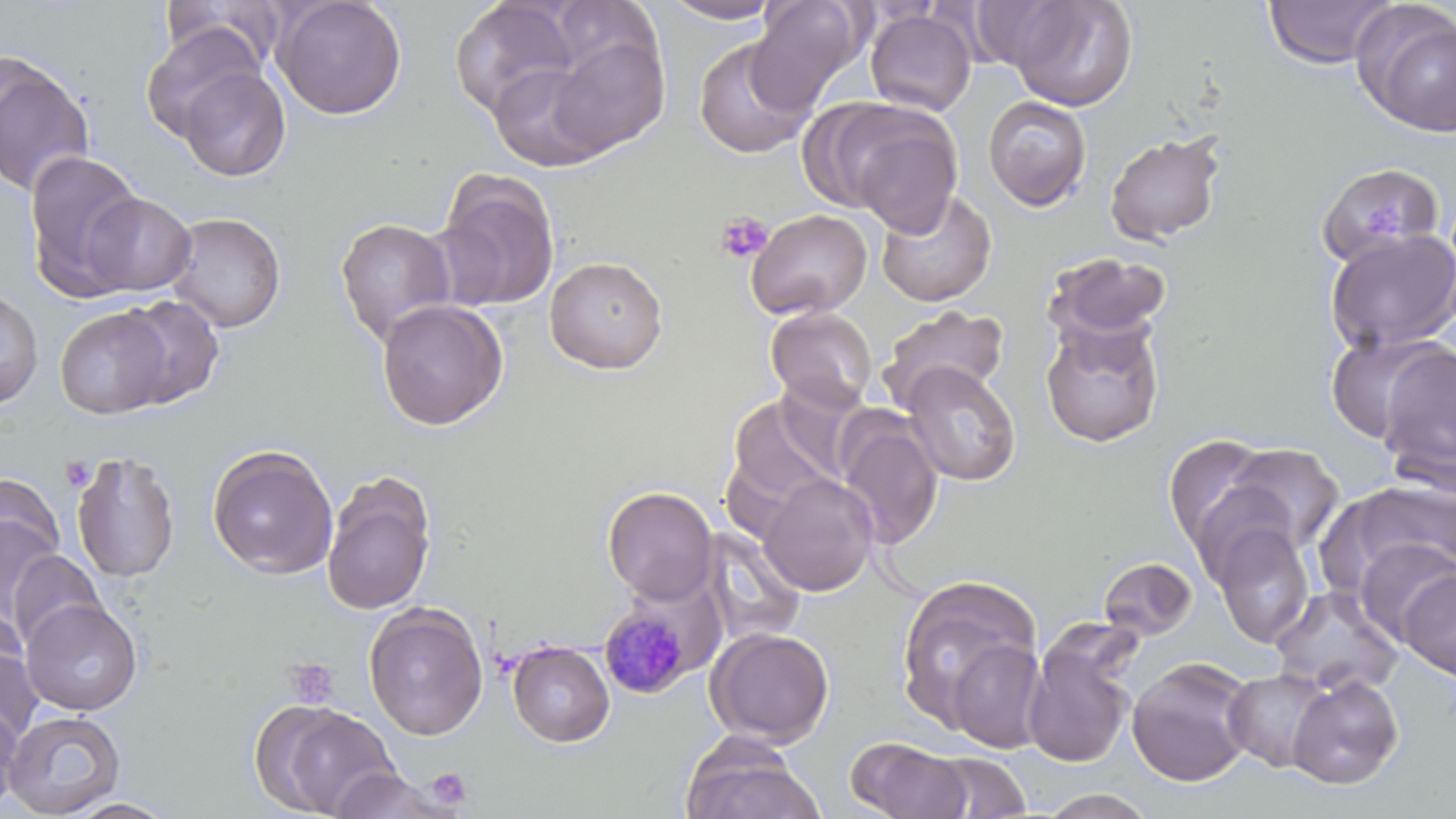

Summary:
  - Coordinate format: approximate bounding boxes as (x1,y1)-(x2,y2) corner pairs in pixels
  - Plasmodium malariae-infected red blood cell locations: (598,603)-(697,700)
  - Uninfected red blood cell locations: (273,0)-(407,120), (657,0)-(783,24), (746,0)-(867,110), (1005,0)-(1139,111), (1263,0)-(1398,69), (161,1)-(290,72), (448,1)-(579,119), (1352,3)-(1456,136), (865,9)-(977,116), (140,22)-(265,143), (541,31)-(671,155), (693,35)-(816,159), (0,51)-(95,198), (488,59)-(609,173), (178,66)-(292,182), (810,95)-(961,224), (982,95)-(1091,211), (1105,131)-(1226,245), (23,149)-(145,299), (1316,162)-(1445,269), (437,170)-(561,311), (875,189)-(997,307), (80,192)-(197,297), (746,208)-(873,320), (165,211)-(286,333), (335,216)-(457,347), (1325,227)-(1456,353), (1043,250)-(1172,344), (545,256)-(668,374), (0,289)-(43,409), (116,294)-(225,409), (376,299)-(508,430), (876,304)-(1011,412), (765,305)-(878,412), (54,306)-(173,419), (1041,317)-(1165,447), (1326,331)-(1451,445), (1377,344)-(1456,489), (901,361)-(1021,486), (726,395)-(845,510), (728,400)-(941,532), (835,411)-(943,550), (1163,434)-(1277,553), (1219,442)-(1346,560), (206,443)-(339,579), (70,449)-(181,583), (320,473)-(436,617), (758,473)-(878,596), (0,474)-(65,572), (1331,479)-(1456,586), (602,486)-(719,603), (0,510)-(64,626), (1210,523)-(1315,648), (699,526)-(807,648), (1354,537)-(1456,644), (5,550)-(106,652), (1098,556)-(1198,641), (1399,569)-(1456,681), (894,575)-(1044,731), (1270,586)-(1403,698), (21,598)-(143,716), (363,602)-(488,741), (0,606)-(29,704), (705,627)-(834,746), (1023,630)-(1139,769), (1,632)-(42,744), (946,639)-(1048,753), (507,640)-(615,747), (1126,656)-(1256,787), (1223,668)-(1334,773), (1286,674)-(1404,790), (255,699)-(400,818), (0,701)-(22,815), (3,709)-(126,817), (847,737)-(972,819), (680,740)-(826,819), (922,752)-(1031,818), (326,767)-(461,819), (1038,789)-(1157,818), (61,797)-(180,818)
  - Platelet locations: (1362,200)-(1409,239), (714,211)-(773,264), (60,456)-(94,491), (283,657)-(338,708), (427,767)-(472,809)
  - Slide-level diagnosis: Plasmodium malariae
  - Preparation: thin blood film
  - Image size: 1456×819 pixels
  - Field of view: one of a larger specimen
  - Stain: May-Grünwald-Giemsa
  - Magnification: 1000x
  - Modality: optical microscopy